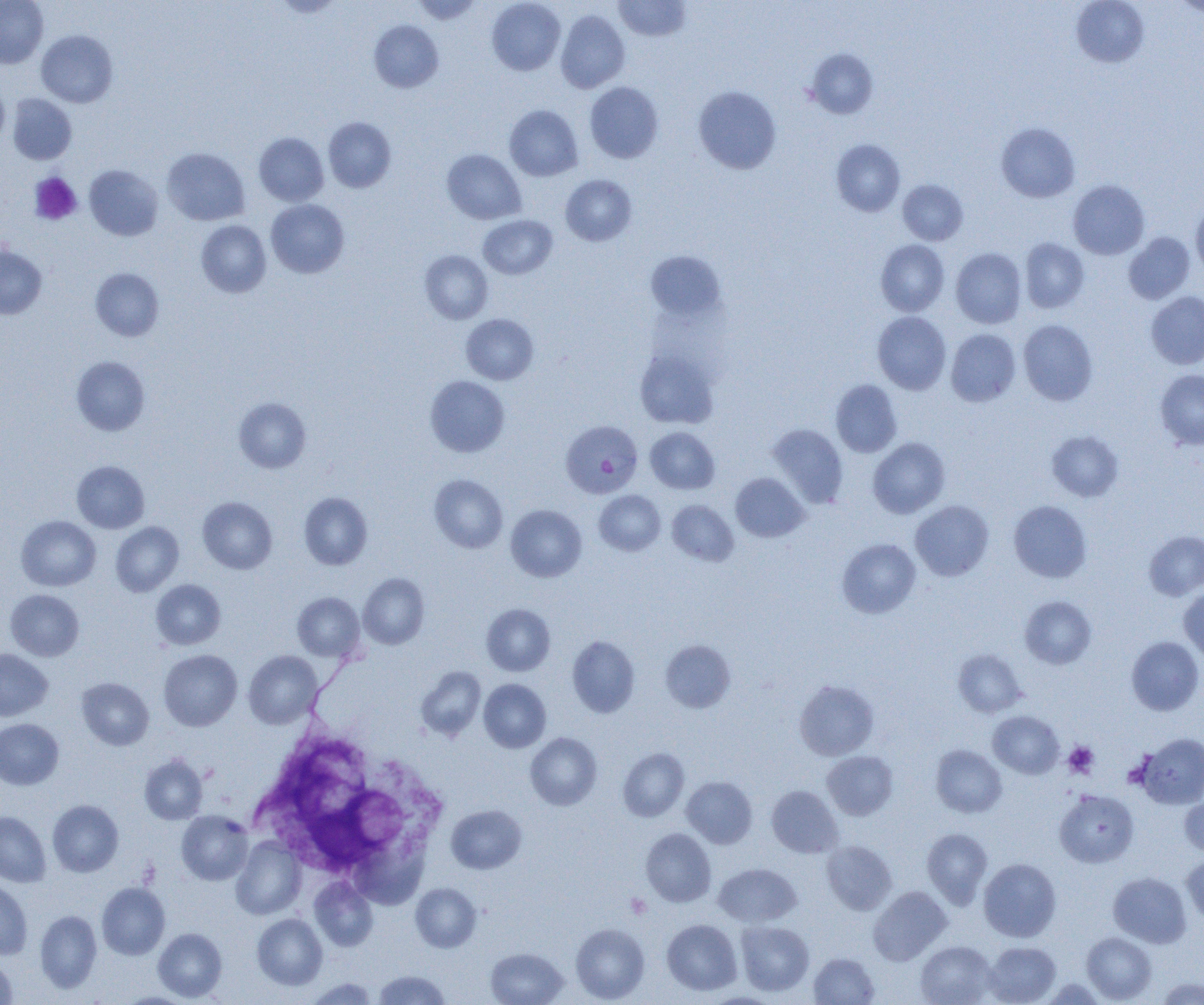

Summary:
  - Coordinate format: approximate bounding boxes as [x1, y1, x2, y2] in pixels
  - Uninfected red blood cell locations: [0, 0, 48, 68], [272, 0, 344, 18], [411, 0, 483, 24], [487, 0, 565, 75], [614, 0, 691, 42], [1071, 0, 1150, 68], [1170, 0, 1204, 17], [556, 10, 630, 93], [369, 20, 444, 92], [36, 30, 118, 107], [804, 48, 878, 119], [0, 82, 9, 147], [584, 82, 664, 163], [693, 86, 782, 174], [8, 94, 76, 164], [504, 105, 583, 181], [324, 117, 396, 192], [996, 122, 1080, 203], [254, 132, 329, 206], [831, 139, 905, 217], [162, 147, 250, 225], [442, 149, 526, 224], [84, 165, 163, 240], [560, 174, 636, 246], [898, 179, 968, 245], [1068, 180, 1150, 259], [266, 199, 349, 278], [1191, 202, 1204, 280], [478, 215, 558, 279], [196, 220, 271, 297], [1124, 232, 1195, 304], [1020, 238, 1089, 313], [876, 240, 950, 316], [0, 243, 47, 319], [951, 248, 1026, 328], [420, 250, 493, 324], [645, 250, 726, 321], [90, 268, 164, 341], [1146, 291, 1204, 369], [872, 312, 951, 394], [461, 314, 539, 385], [1018, 319, 1098, 405], [946, 328, 1021, 406], [634, 348, 719, 429], [71, 356, 150, 436], [1155, 370, 1204, 450], [425, 375, 509, 457], [831, 380, 902, 457], [234, 397, 311, 473], [768, 423, 848, 507], [645, 426, 720, 494], [1047, 430, 1123, 502], [868, 437, 950, 518], [71, 460, 150, 533], [731, 473, 809, 542], [429, 474, 508, 553], [594, 490, 665, 555], [299, 492, 373, 570], [198, 497, 277, 574], [667, 499, 739, 566], [910, 500, 994, 581], [1009, 500, 1091, 582], [506, 505, 587, 581], [16, 515, 101, 591], [111, 522, 184, 596], [1144, 530, 1204, 600], [837, 538, 921, 618], [358, 573, 429, 649], [151, 579, 226, 650], [1179, 588, 1204, 661], [5, 589, 84, 661], [292, 592, 365, 661], [1019, 596, 1096, 669], [481, 603, 555, 676], [567, 635, 639, 717], [1126, 636, 1203, 715], [661, 639, 735, 713], [0, 649, 52, 721], [953, 649, 1026, 717], [159, 650, 242, 731], [244, 650, 322, 729], [415, 666, 486, 741], [77, 678, 154, 750], [478, 679, 551, 753], [794, 679, 879, 760], [988, 711, 1063, 778], [0, 718, 63, 790], [525, 732, 602, 810], [1137, 733, 1204, 808], [931, 744, 1007, 818], [618, 748, 689, 821], [822, 751, 898, 820], [139, 755, 208, 824], [682, 776, 757, 848], [767, 785, 842, 858], [1055, 790, 1138, 867], [1180, 794, 1204, 856], [47, 800, 123, 876], [446, 804, 526, 874], [176, 810, 253, 885], [0, 811, 51, 887], [641, 828, 716, 906], [922, 828, 992, 908], [231, 837, 306, 919], [821, 841, 896, 915], [350, 845, 435, 912], [1182, 855, 1204, 924], [979, 858, 1061, 942], [713, 863, 801, 926], [1109, 872, 1191, 948], [309, 877, 378, 951], [0, 879, 32, 959], [410, 882, 481, 953], [96, 883, 170, 959], [869, 886, 951, 965], [35, 910, 102, 993], [252, 913, 328, 989], [662, 919, 742, 995], [736, 920, 814, 996], [571, 924, 650, 1003], [153, 928, 227, 1001], [1082, 932, 1156, 1003], [915, 940, 997, 1005], [984, 942, 1061, 1005], [485, 947, 568, 1005], [809, 953, 879, 1005], [0, 956, 17, 1003], [374, 970, 450, 1004], [306, 977, 379, 1004], [1156, 977, 1204, 1004], [1038, 979, 1108, 1004], [116, 992, 195, 1005], [702, 993, 782, 1005]
  - Platelet locations: [29, 173, 82, 226], [1063, 741, 1098, 777], [625, 894, 651, 918]
  - White blood cell locations: [249, 733, 420, 878]
  - Plasmodium falciparum-infected red blood cell locations: [561, 420, 643, 498]
  - Slide-level diagnosis: Plasmodium falciparum
  - Field of view: single
  - Magnification: 1000x
  - Image size: 1204×1005 pixels
  - Modality: light microscopy
  - Preparation: thin blood film